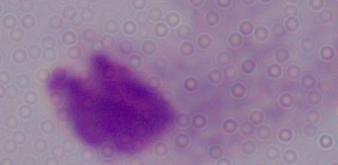
{
  "magnification": "1000x",
  "identification": "trichomonad",
  "modality": "photomicrograph"
}